Describe the morphology of the erythrocytes.
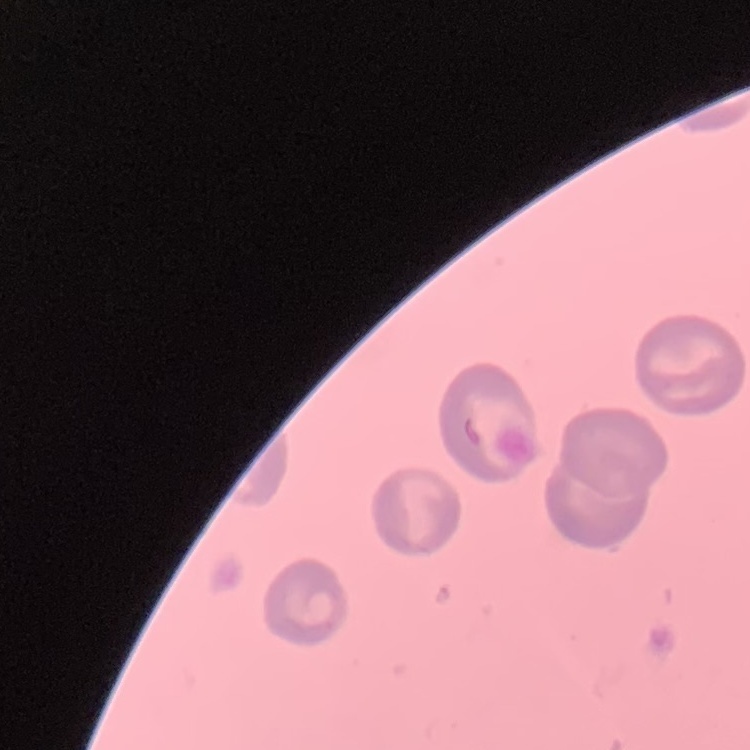

No rouleaux formation.

One tile cut from a larger photomicrograph. Thin blood film. Stained with either Field's or Giemsa.